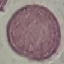

Summary:
  - Result: negative for malaria parasites
  - Stain: Giemsa
  - Image type: cell patch, automatically extracted from a larger field of view and resized to 64 × 64 pixels
  - Capture: smartphone through the microscope eyepiece
  - Preparation: thin smear